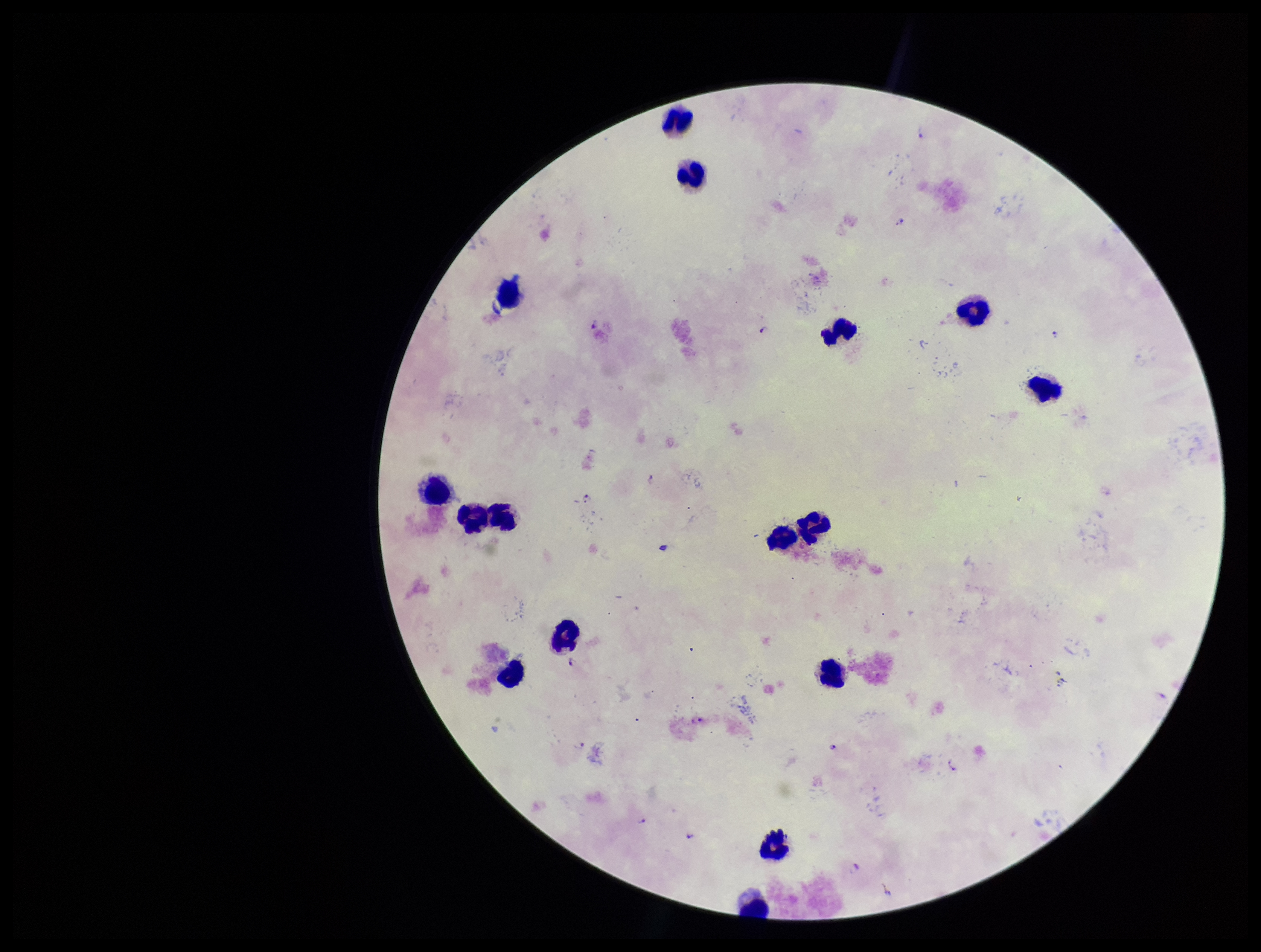
Summary:
  - Species reported for this patient: Plasmodium falciparum
  - Parasite count: 3
  - Stain: Giemsa
  - Field of view: one from this slide
  - Patient malaria status: positive
  - Plasmodium parasites: identified
  - Image size: 1261×952 pixels
  - Leukocyte count: 16
  - Preparation: thick smear
  - Capture: smartphone photograph through the microscope eyepiece